Assess this cell for malaria.
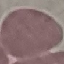
Uninfected.

capture = smartphone through the microscope eyepiece
preparation = thin blood smear
stain = Giemsa
image type = cell patch, automatically extracted from a larger field of view and resized to 64 × 64 pixels